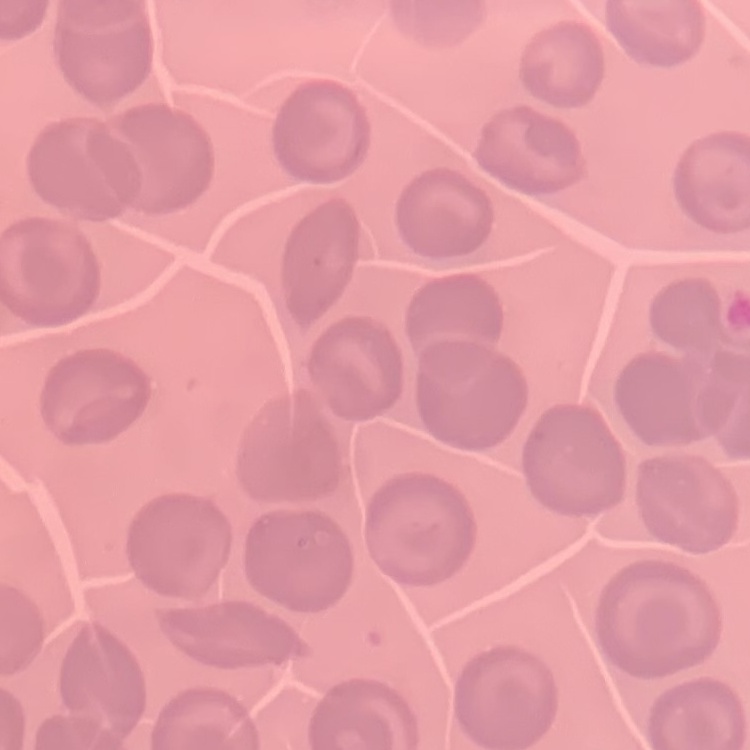

{
  "red_blood_cell_morphology": "no rouleaux formation",
  "image_type": "square crop of a larger photomicrograph",
  "preparation": "thin blood smear",
  "stain": "Field's or Giemsa"
}